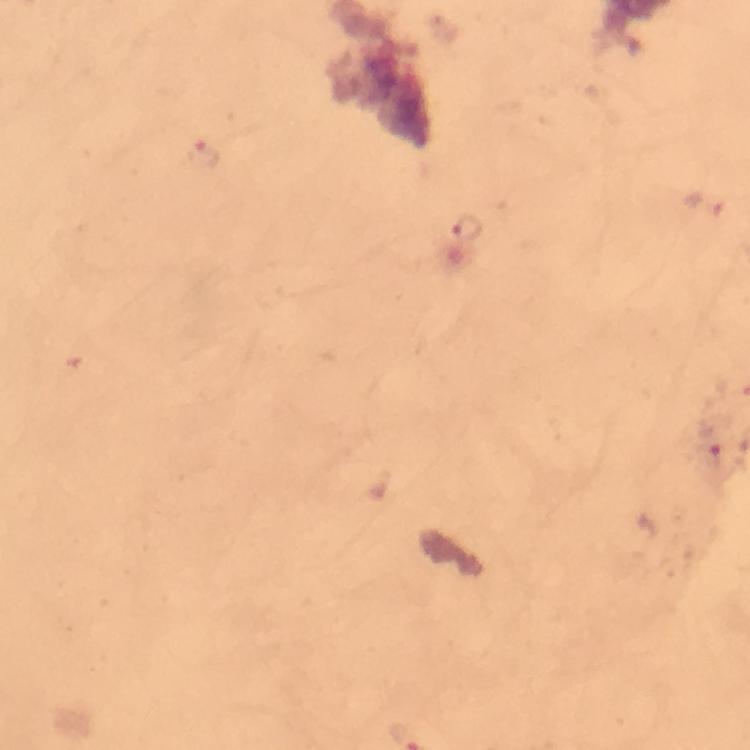
Approximate centers as (x, y) in pixels.
Summary:
  - Malaria parasite locations: (203, 153), (467, 227), (712, 449)
  - Stain: Giemsa
  - Context: from a malaria diagnostic workup
  - Cropped from: a single field of view
  - Capture: smartphone photograph through a microscope
  - Preparation: thick blood film
  - Immersion oil: applied
  - Magnification: 100x
  - Image size: 750×750 pixels